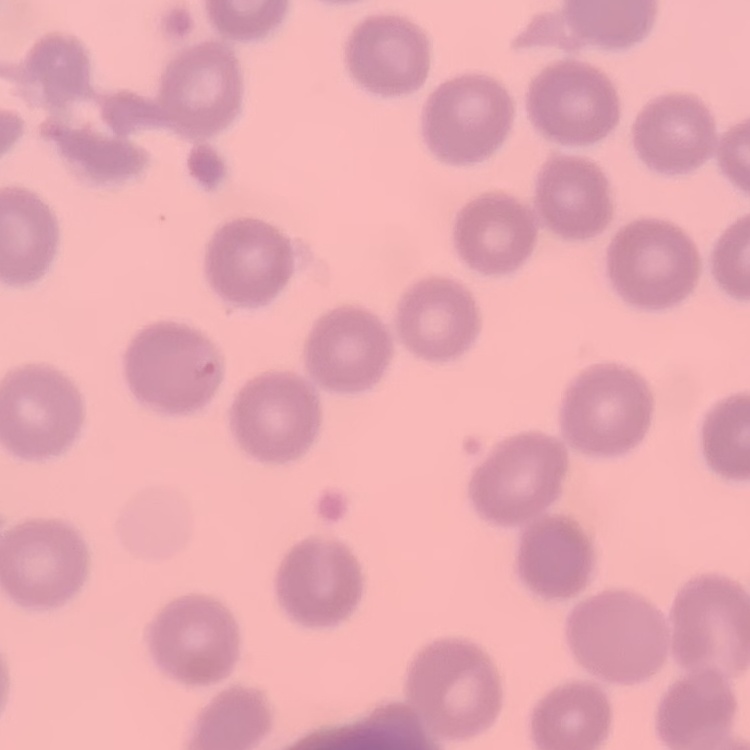
Summary:
  - Erythrocyte morphology: no rouleaux formation
  - Preparation: thin blood film
  - Stain: Field's or Giemsa
  - Image type: square crop of a larger photomicrograph